Assess this cell for malaria.
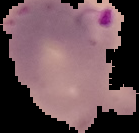

It is parasitized.

image type = cell region segmented out of the field of view; surrounding area masked to black
image size = 139×133 pixels
preparation = thin blood smear